Locate every Plasmodium parasite.
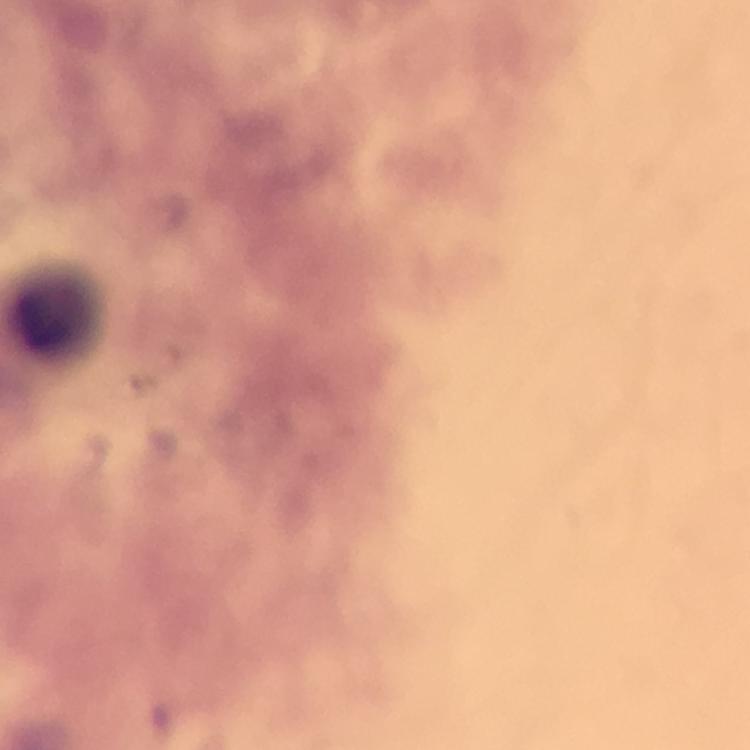

No Plasmodium parasites seen.

Approximate centers as {x, y} in pixels. Leukocyte locations: {59, 312}. Immersion oil was used. Smartphone photograph taken through a microscope. At 100x magnification. Cropped region of a single field of view. Thick smear. Image is 750×750 pixels. Giemsa-stained preparation. From a diagnostic examination for malaria.